Report the malaria status of this cell.
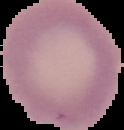
Uninfected.

image size = 124×130 pixels
image type = segmented cell region with the area outside set to black
preparation = thin blood smear